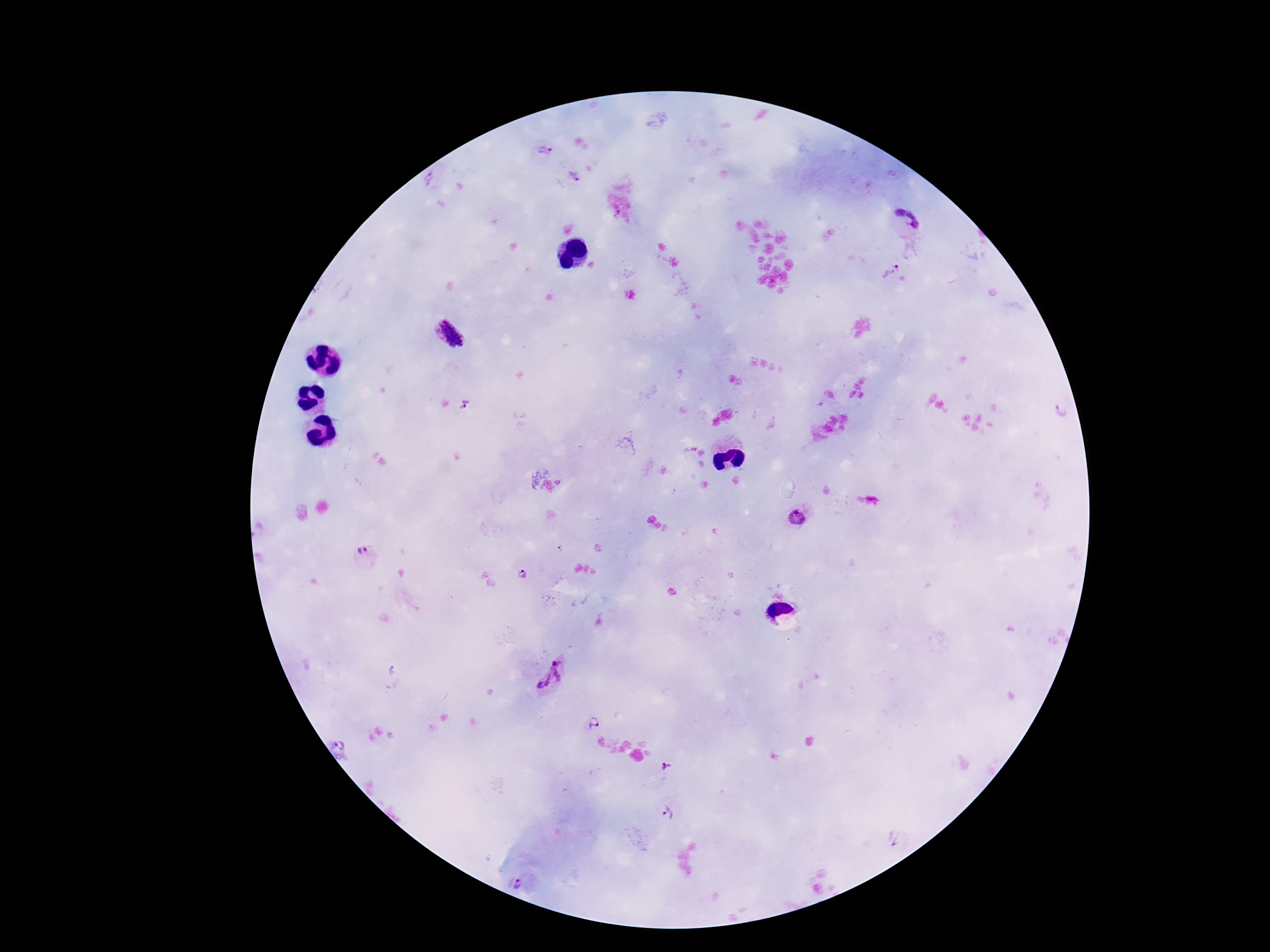 Approximate centers as [x, y] in pixels. Plasmodium parasite locations: [544, 152], [574, 175], [431, 179], [907, 220], [892, 270], [451, 334], [467, 405], [1062, 411], [798, 519], [560, 551], [364, 554], [523, 575], [551, 676], [596, 723], [341, 746], [667, 769], [667, 813], [894, 839], [519, 882]. Thick blood film. Smartphone photograph taken through the microscope eyepiece. Giemsa-stained preparation. Image is 1270×952 pixels. Patient malaria status: infected. Single field of view. 100x magnification.